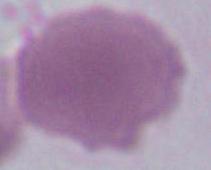
Summary:
  - Magnification: 1000x
  - Modality: photomicrograph
  - Identification: erythrocyte